Describe the morphology of the erythrocytes.
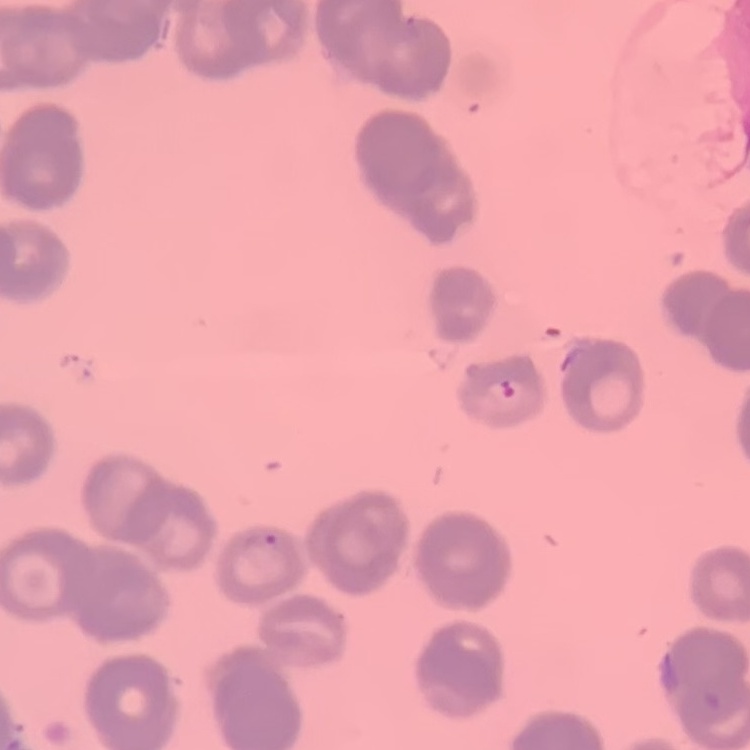

They show rouleaux formation.

Summary:
  - Preparation: thin peripheral smear
  - Stain: Field's or Giemsa
  - Image type: square crop of a larger photomicrograph